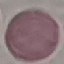
Summary:
  - Result: no malaria parasites detected
  - Image type: automatically extracted cell patch, resized to 64 × 64 pixels
  - Stain: Giemsa
  - Preparation: thin blood film
  - Capture: smartphone camera at the microscope eyepiece